Look for Plasmodium parasites.
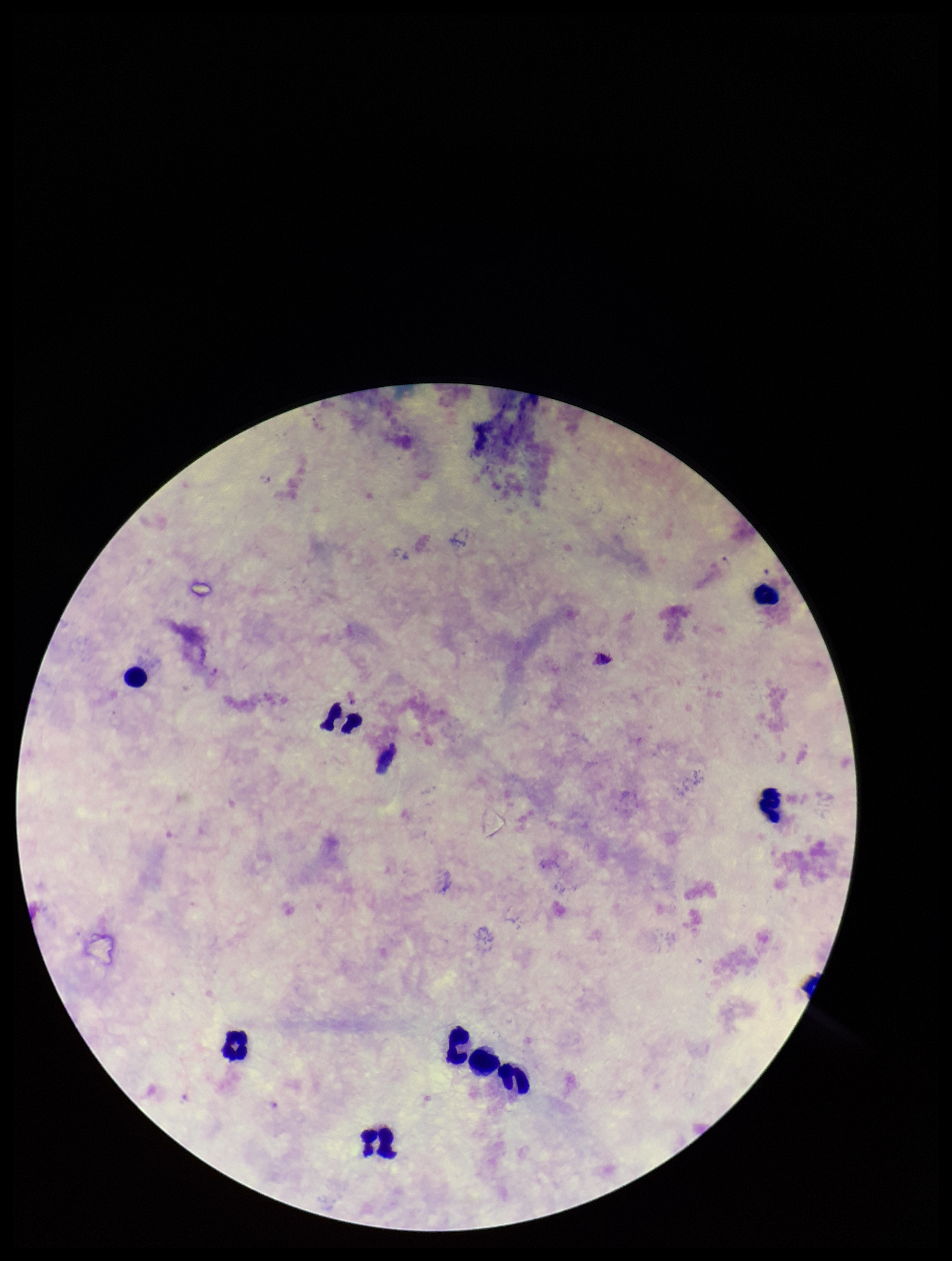
None identified.

Summary:
  - Preparation: thick
  - Stain: Giemsa
  - Species reported for this patient: Plasmodium falciparum
  - Image size: 952×1261 pixels
  - Capture: smartphone photograph through the microscope eyepiece
  - Leukocyte count: 9
  - Parasite count: 0
  - Patient malaria status: positive
  - Field of view: one from this slide